Describe the morphology of the erythrocytes.
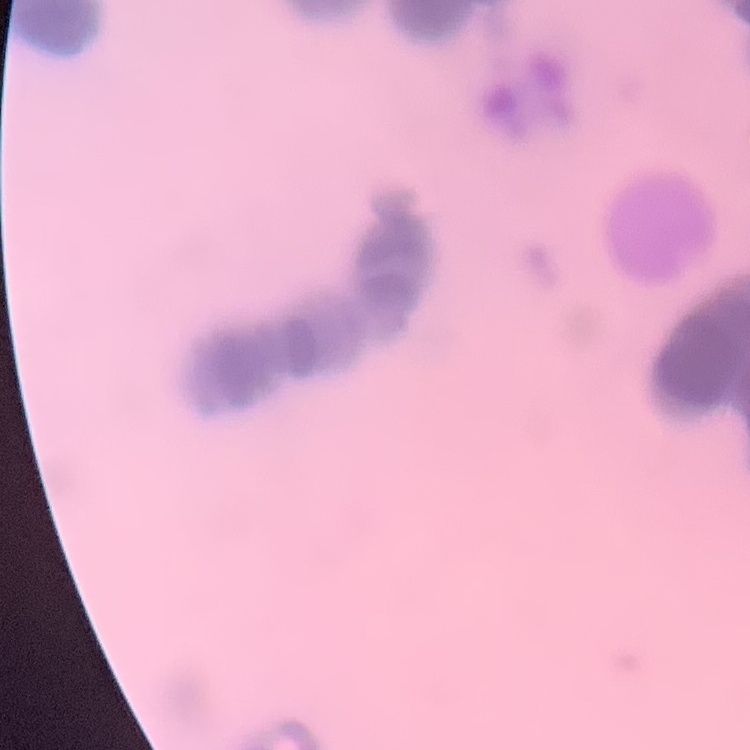

They show rouleaux formation.

Square crop of a larger photomicrograph. Thin peripheral smear. Stained with either Field's or Giemsa.